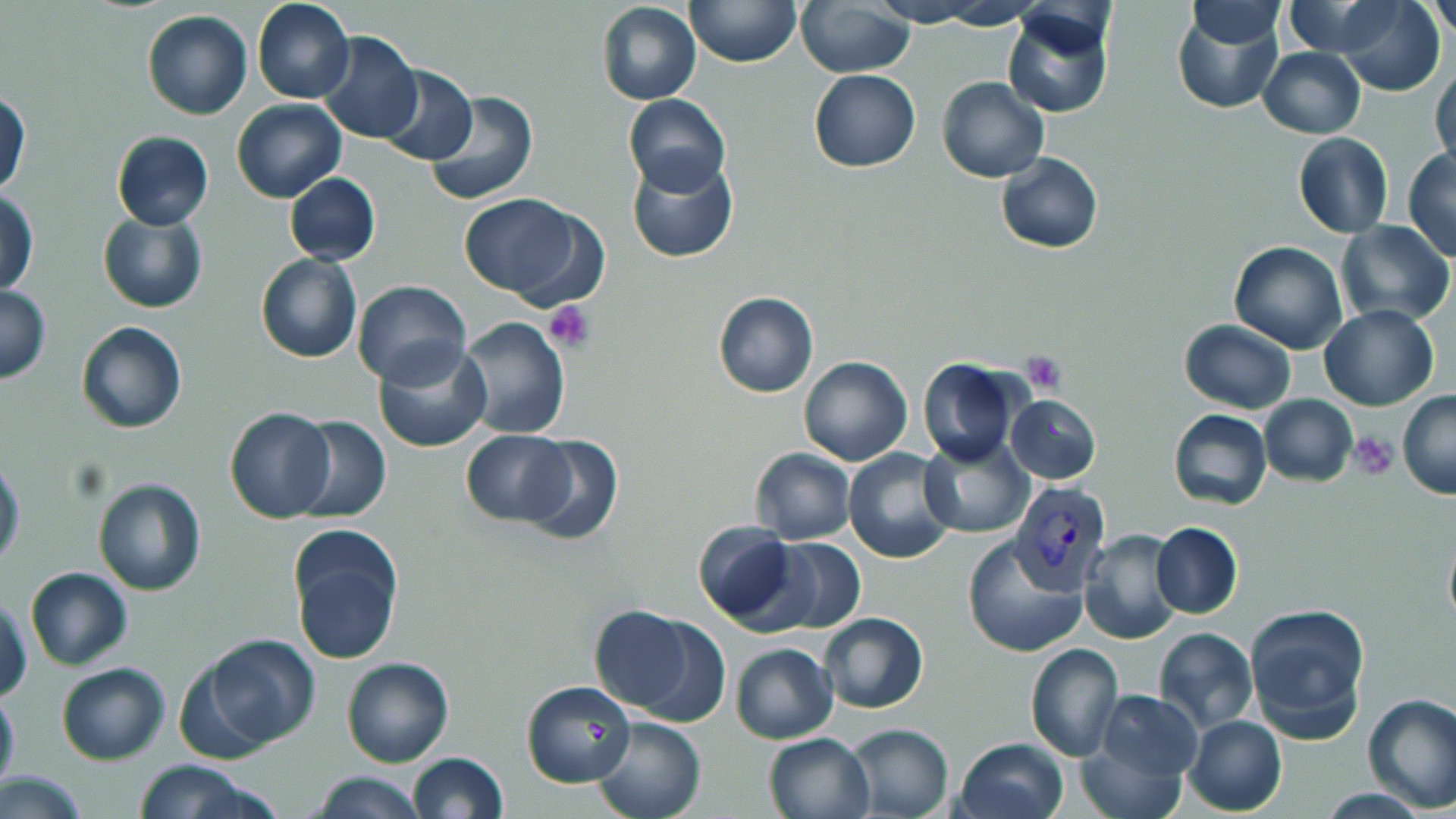

Summary:
  - Coordinate format: approximate bounding boxes as [x1, y1, x2, y2] in pixels
  - Uninfected red blood cell locations: [253, 0, 355, 103], [685, 0, 801, 67], [795, 0, 916, 77], [867, 0, 993, 26], [1184, 1, 1287, 48], [1336, 1, 1445, 96], [596, 2, 701, 105], [1428, 2, 1455, 40], [1002, 6, 1116, 119], [1171, 7, 1284, 114], [142, 10, 252, 119], [317, 32, 423, 144], [1260, 48, 1364, 138], [1431, 63, 1456, 170], [375, 65, 477, 166], [810, 70, 921, 171], [937, 75, 1049, 183], [1, 89, 31, 197], [424, 91, 537, 206], [623, 93, 731, 199], [230, 98, 346, 203], [111, 130, 214, 229], [1293, 133, 1393, 238], [1403, 147, 1456, 261], [625, 152, 740, 263], [995, 152, 1102, 254], [284, 174, 381, 265], [1, 189, 38, 296], [459, 194, 597, 300], [98, 212, 207, 313], [1336, 220, 1455, 328], [1227, 241, 1347, 354], [254, 253, 362, 363], [352, 280, 471, 389], [1, 284, 50, 382], [713, 291, 817, 398], [1319, 306, 1439, 410], [459, 316, 571, 438], [1179, 320, 1296, 414], [75, 321, 187, 433], [373, 340, 491, 453], [799, 356, 912, 466], [916, 357, 1022, 468], [1396, 391, 1456, 499], [1005, 394, 1101, 484], [1259, 394, 1358, 487], [224, 407, 336, 523], [1167, 409, 1273, 511], [289, 414, 390, 523], [461, 430, 572, 525], [512, 433, 624, 546], [918, 437, 1032, 539], [842, 447, 957, 564], [751, 448, 855, 543], [0, 456, 24, 571], [93, 478, 206, 595], [693, 521, 802, 628], [1151, 522, 1242, 619], [287, 526, 404, 664], [1442, 526, 1456, 633], [1077, 529, 1186, 646], [960, 535, 1087, 658], [762, 537, 866, 636], [34, 564, 143, 765], [26, 567, 132, 670], [1, 596, 32, 703], [1242, 601, 1369, 743], [587, 606, 700, 715], [818, 613, 930, 712], [626, 616, 730, 727], [1154, 627, 1257, 734], [731, 632, 930, 732], [204, 635, 321, 748], [1025, 642, 1124, 761], [730, 643, 838, 744], [342, 657, 452, 768], [171, 658, 274, 765], [56, 662, 170, 765], [520, 678, 636, 788], [0, 686, 19, 795], [1091, 691, 1205, 792], [1361, 693, 1456, 810], [589, 715, 707, 819], [1184, 715, 1287, 815], [844, 722, 954, 819], [763, 731, 874, 818], [955, 737, 1069, 819], [407, 752, 509, 819], [128, 761, 270, 819], [0, 768, 88, 818], [310, 773, 428, 818]
  - Plasmodium vivax-infected red blood cell locations: [1008, 479, 1112, 593]
  - Platelet locations: [547, 301, 598, 353], [1020, 352, 1067, 392], [1349, 433, 1398, 479]
  - Slide-level diagnosis: Plasmodium vivax
  - Preparation: thin blood smear
  - Image size: 1456×819 pixels
  - Field of view: one of a larger specimen
  - Modality: light microscopy
  - Stain: May-Grünwald-Giemsa
  - Magnification: 1000x